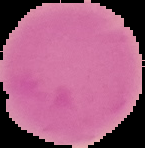

Segmented cell region on a black background. From a thin blood smear. Malaria status: uninfected. Image is 145×148 pixels.